Name the blood parasite species.
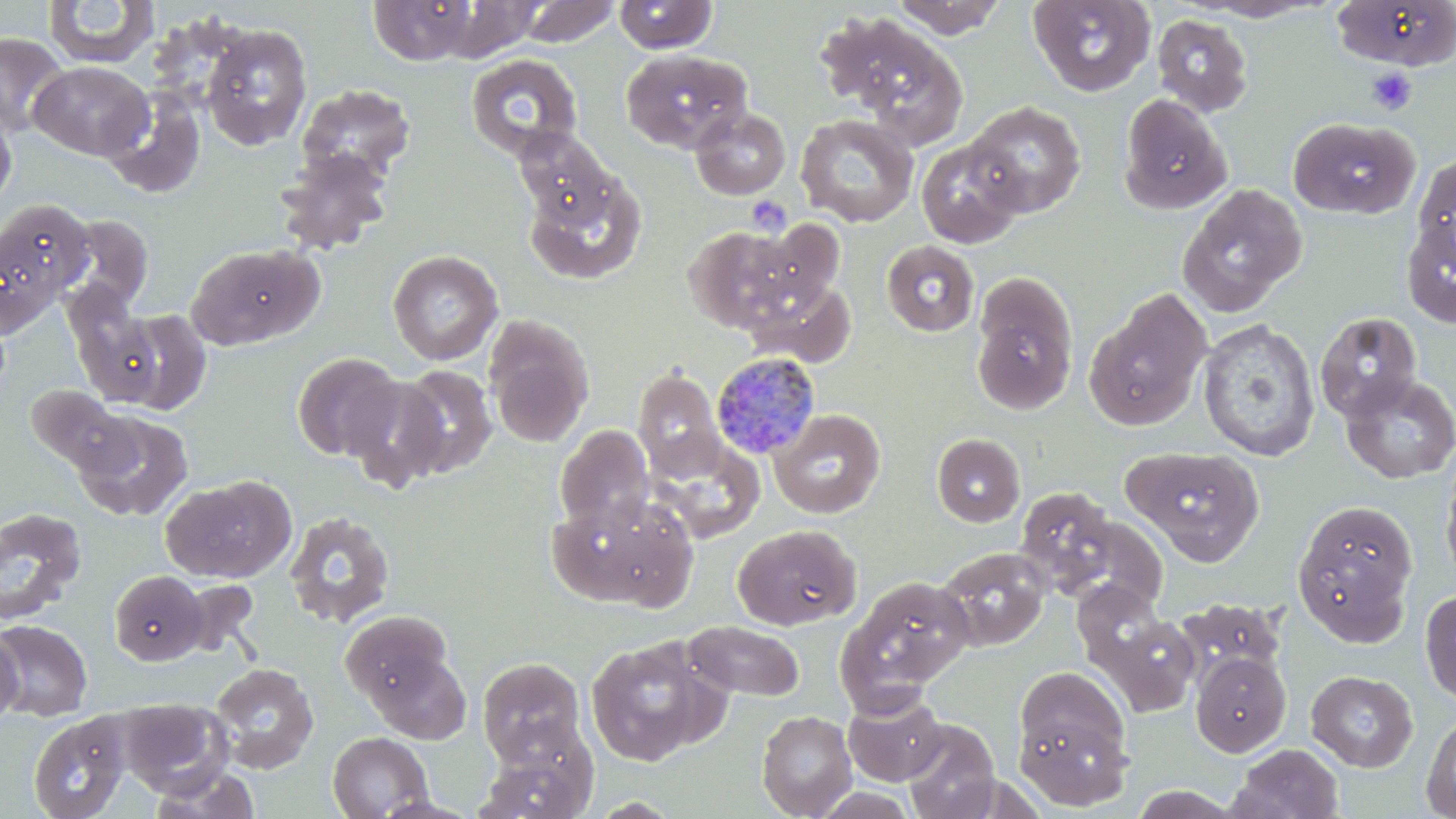

Plasmodium malariae.

Approximate bounding boxes as (x1, y1, x2, y2) in pixels. Plasmodium malariae-infected red blood cell locations: (713, 352, 823, 460). Platelet locations: (1367, 67, 1417, 115), (746, 196, 791, 237). Uninfected red blood cell locations: (43, 0, 160, 68), (517, 0, 620, 47), (889, 0, 1008, 38), (1028, 0, 1156, 96), (1189, 0, 1333, 22), (1330, 0, 1456, 70), (368, 1, 478, 65), (613, 1, 718, 54), (817, 12, 969, 146), (1151, 15, 1253, 116), (201, 24, 312, 150), (0, 31, 70, 137), (621, 48, 753, 152), (465, 53, 583, 161), (29, 61, 153, 160), (296, 84, 416, 183), (103, 89, 205, 199), (1118, 94, 1232, 214), (964, 100, 1086, 217), (689, 106, 791, 200), (0, 110, 16, 207), (795, 114, 919, 228), (1287, 117, 1420, 219), (513, 128, 620, 228), (915, 137, 1027, 248), (273, 148, 394, 256), (1412, 151, 1456, 269), (523, 165, 647, 287), (1177, 183, 1308, 317), (0, 200, 94, 311), (65, 215, 153, 310), (1401, 216, 1456, 328), (743, 221, 844, 313), (683, 224, 802, 333), (881, 240, 979, 337), (187, 244, 321, 349), (387, 249, 503, 365), (970, 273, 1079, 416), (744, 278, 857, 367), (1085, 289, 1213, 431), (110, 309, 212, 413), (1315, 312, 1422, 421), (484, 314, 595, 447), (1197, 319, 1321, 462), (291, 352, 404, 461), (394, 365, 497, 479), (633, 367, 726, 479), (1340, 373, 1456, 484), (342, 375, 448, 491), (24, 383, 136, 478), (769, 408, 885, 518), (73, 410, 193, 522), (555, 425, 655, 533), (932, 433, 1025, 527), (647, 436, 764, 543), (1124, 446, 1265, 565), (1441, 460, 1456, 588), (160, 479, 293, 582), (1015, 486, 1119, 594), (547, 493, 697, 610), (1291, 499, 1419, 642), (0, 507, 86, 625), (284, 510, 395, 629), (733, 524, 861, 630), (936, 547, 1050, 651), (109, 570, 206, 665), (841, 576, 976, 699), (1420, 589, 1456, 706), (1175, 598, 1284, 688), (340, 610, 452, 706), (1096, 613, 1200, 716), (0, 620, 93, 720), (684, 621, 804, 701), (0, 625, 23, 730), (584, 637, 716, 765), (368, 651, 471, 745), (1190, 652, 1291, 757), (477, 657, 585, 765), (209, 663, 319, 774), (1013, 664, 1134, 793), (1306, 670, 1419, 772), (842, 690, 948, 786), (117, 698, 232, 795), (1421, 709, 1456, 818), (757, 710, 858, 818), (28, 713, 131, 819), (900, 718, 1001, 819), (327, 731, 433, 818), (478, 737, 597, 818), (1228, 744, 1344, 819), (147, 768, 262, 819). May-Grünwald-Giemsa stain. Optical microscopy. Thin blood smear. Image is 1456×819 pixels. Captured at 1000x magnification. One field of a larger specimen.